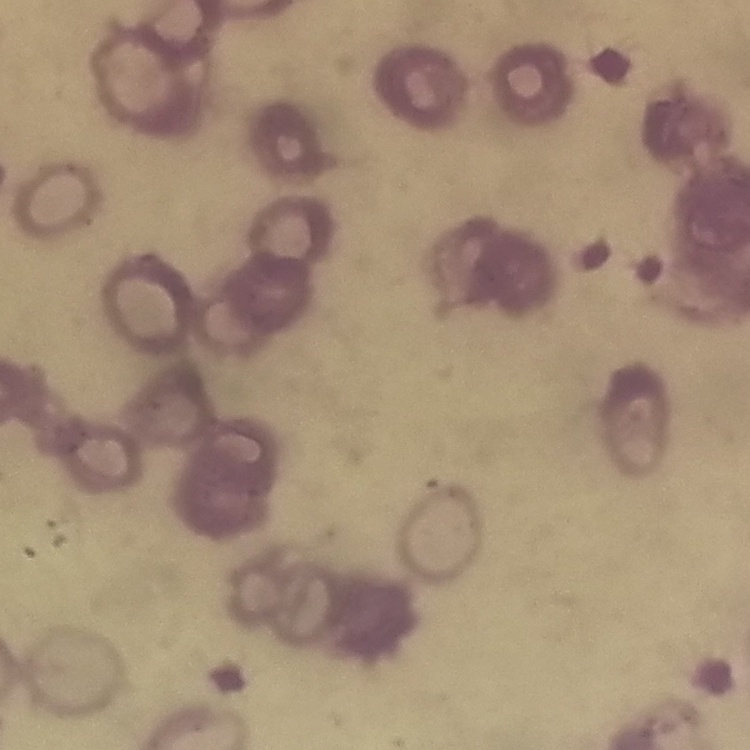

The erythrocytes exhibit rouleaux formation. One tile cut from a larger photomicrograph. Thin peripheral smear. Field's or Giemsa stain.